Classify this cell by malaria status.
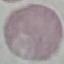
Uninfected.

Thin smear of blood. Automatically extracted cell patch, resized to 64 × 64 pixels. Giemsa stain. Photographed with a smartphone camera at the microscope eyepiece.